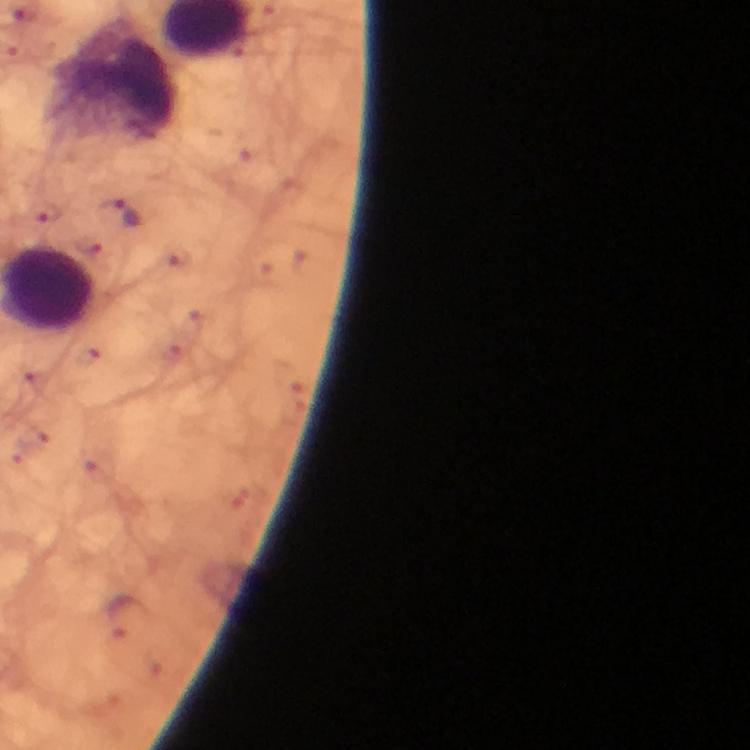
leukocyte locations = approximate object centers, in pixels from the top-left corner: (x=116, y=86)
malaria parasite locations = approximate object centers, in pixels from the top-left corner: (x=117, y=214), (x=125, y=618)
cropped from = a single field of view
magnification = 100x
image size = 750×750 pixels
immersion oil = applied
context = from a malaria diagnostic workup
preparation = thick smear
stain = Giemsa
capture = smartphone photograph through a microscope